Classify this cell by malaria status.
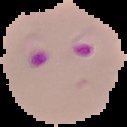
Parasitized.

Image is 127×127 pixels. Segmented cell region on a black background. From a thin blood film.